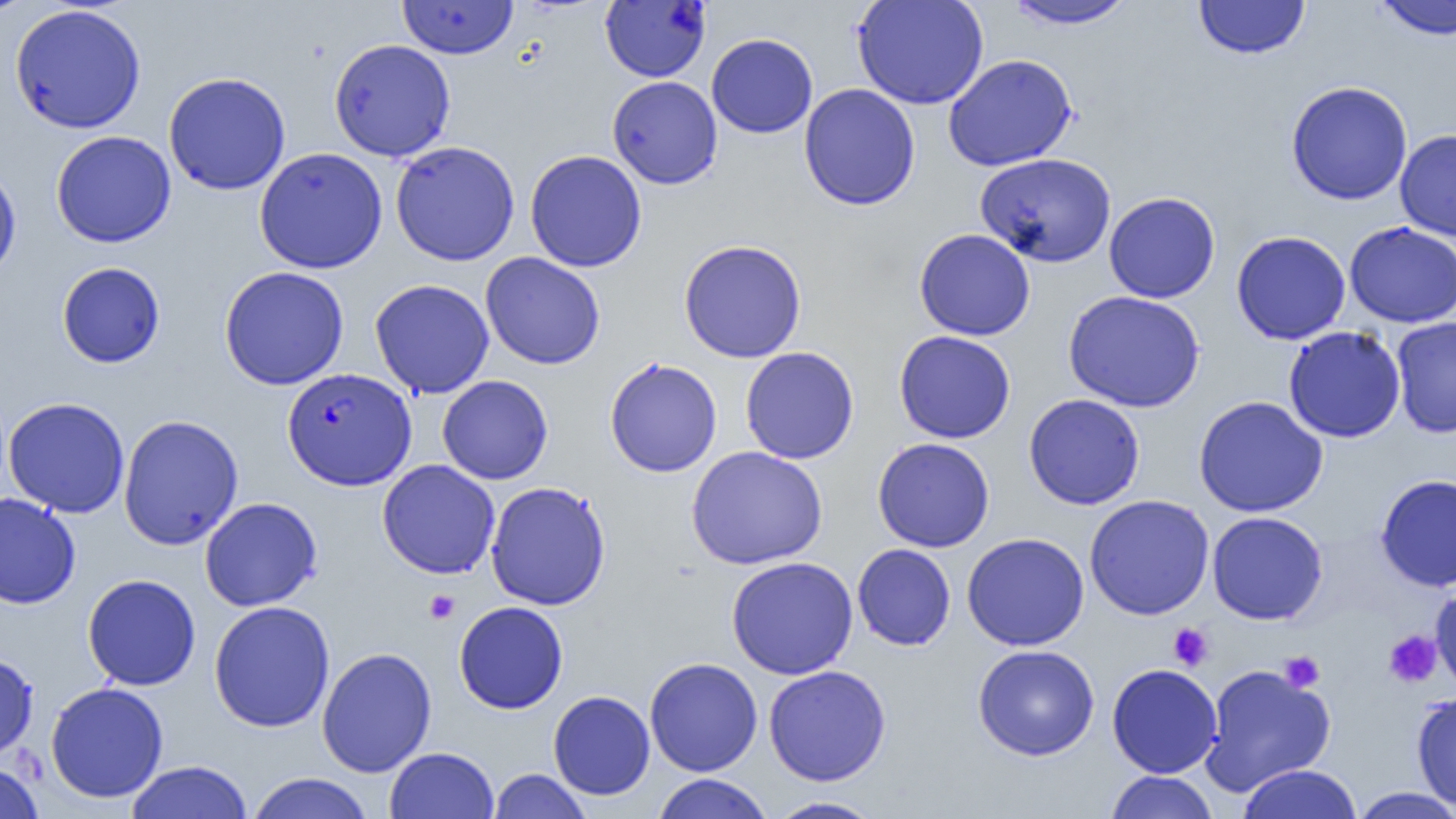
Summary:
  - Coordinate format: approximate bounding boxes as [x1, y1, x2, y2] in pixels
  - Plasmodium falciparum-infected red blood cell locations (subset): [282, 367, 417, 491]
  - Platelet locations: [424, 590, 459, 624], [1167, 623, 1214, 670], [1383, 629, 1442, 688], [1278, 651, 1325, 692]
  - Uninfected red blood cell locations (subset): [0, 0, 38, 19], [851, 0, 989, 111], [1002, 0, 1139, 29], [1371, 0, 1456, 41], [398, 1, 518, 59], [1194, 1, 1310, 60], [9, 4, 147, 134], [706, 33, 818, 138], [328, 39, 456, 161], [943, 53, 1078, 172], [163, 71, 291, 195], [607, 75, 723, 189], [1285, 81, 1413, 205], [798, 83, 921, 210], [1395, 128, 1456, 241], [50, 131, 176, 248], [390, 140, 521, 266], [254, 147, 388, 274], [524, 150, 647, 272], [975, 152, 1117, 267], [0, 162, 22, 284], [1104, 192, 1220, 303], [1344, 221, 1456, 328], [914, 228, 1036, 341], [1231, 230, 1351, 345], [678, 239, 807, 363], [480, 252, 605, 369], [56, 261, 165, 368], [218, 266, 349, 390], [369, 279, 495, 399], [1063, 290, 1205, 413], [1390, 316, 1456, 439], [1283, 326, 1406, 442], [893, 330, 1016, 444], [740, 347, 859, 464], [604, 357, 722, 478], [437, 375, 553, 484], [1023, 393, 1145, 510], [1193, 395, 1328, 517], [2, 397, 131, 518], [119, 414, 244, 550], [872, 437, 995, 552], [686, 446, 828, 569], [377, 459, 500, 579], [1375, 474, 1456, 592], [485, 480, 612, 611], [0, 492, 81, 609], [1084, 494, 1215, 620], [199, 497, 323, 611], [1207, 511, 1328, 625], [961, 532, 1089, 651], [852, 544, 956, 651], [725, 557, 859, 679], [82, 574, 201, 691], [1430, 582, 1456, 696], [209, 601, 335, 732], [454, 601, 568, 714], [973, 644, 1100, 761], [316, 647, 437, 777], [0, 651, 39, 761], [644, 658, 763, 776], [1106, 663, 1223, 778], [1199, 664, 1336, 796], [763, 665, 891, 786], [45, 682, 168, 803], [548, 690, 655, 800], [1411, 692, 1456, 811], [384, 747, 500, 819], [125, 760, 254, 819], [0, 761, 45, 819], [1236, 763, 1363, 819], [488, 768, 592, 819], [1104, 771, 1219, 818], [246, 772, 375, 819], [651, 774, 774, 819], [1349, 787, 1456, 818], [766, 796, 884, 818]
  - Slide-level diagnosis: Plasmodium falciparum
  - Preparation: thin blood smear
  - Modality: optical microscopy
  - Field of view: one of a larger specimen
  - Image size: 1456×819 pixels
  - Magnification: 1000x